State which parasite is depicted.
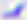
This is Toxoplasma gondii.

Summary:
  - Modality: photomicrograph
  - Magnification: 400x